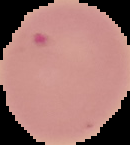
malaria status = parasitized
preparation = thin blood smear
image type = cell region segmented out of the field of view; surrounding area masked to black
image size = 130×145 pixels